Locate and identify every blood parasite.
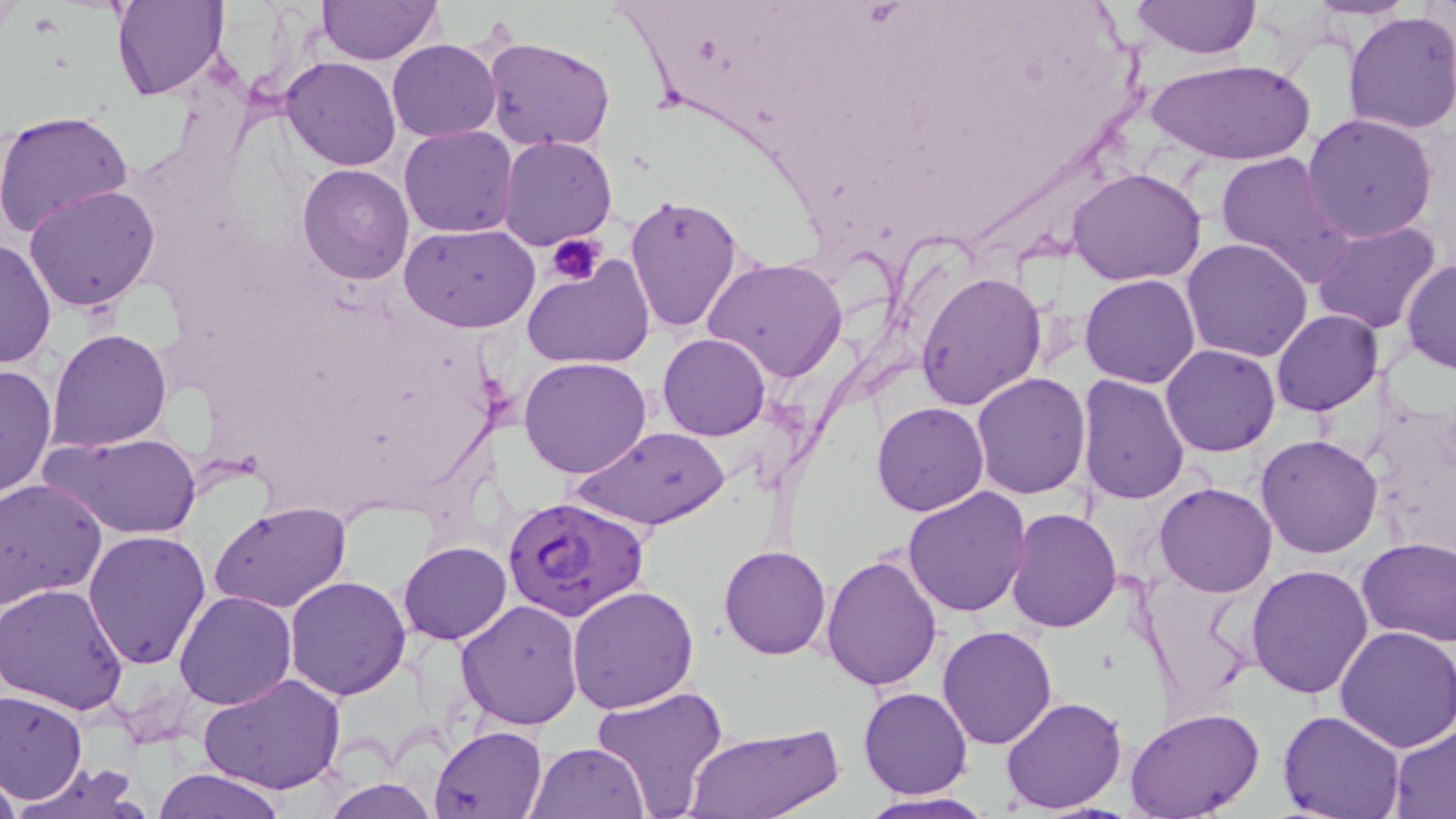

Approximate bounding boxes as named x1/y1/x2/y2 corners in pixels.
Plasmodium falciparum-infected red blood cells: (x1=502, y1=493, x2=651, y2=624).
No Plasmodium ovale, Plasmodium malariae, Plasmodium vivax, Babesia divergens, or Trypanosoma brucei observed.

Uninfected red blood cell locations: (x1=111, y1=1, x2=227, y2=101), (x1=315, y1=1, x2=443, y2=65), (x1=1128, y1=2, x2=1261, y2=59), (x1=1341, y1=10, x2=1456, y2=135), (x1=484, y1=36, x2=617, y2=153), (x1=387, y1=37, x2=501, y2=142), (x1=281, y1=57, x2=401, y2=171), (x1=1145, y1=57, x2=1314, y2=167), (x1=0, y1=108, x2=134, y2=238), (x1=1301, y1=113, x2=1439, y2=243), (x1=399, y1=124, x2=520, y2=237), (x1=498, y1=135, x2=617, y2=250), (x1=1213, y1=151, x2=1356, y2=290), (x1=298, y1=163, x2=414, y2=284), (x1=1067, y1=166, x2=1209, y2=286), (x1=24, y1=185, x2=160, y2=311), (x1=625, y1=193, x2=747, y2=333), (x1=1311, y1=221, x2=1442, y2=335), (x1=400, y1=222, x2=540, y2=333), (x1=0, y1=236, x2=56, y2=371), (x1=1181, y1=237, x2=1314, y2=362), (x1=522, y1=254, x2=656, y2=371), (x1=703, y1=257, x2=848, y2=384), (x1=1401, y1=257, x2=1455, y2=374), (x1=915, y1=270, x2=1048, y2=413), (x1=1079, y1=273, x2=1200, y2=389), (x1=1270, y1=309, x2=1384, y2=415), (x1=49, y1=328, x2=172, y2=451), (x1=658, y1=333, x2=771, y2=441), (x1=1161, y1=344, x2=1282, y2=457), (x1=1096, y1=351, x2=1232, y2=480), (x1=520, y1=357, x2=654, y2=478), (x1=0, y1=362, x2=57, y2=500), (x1=970, y1=372, x2=1091, y2=499), (x1=1077, y1=373, x2=1190, y2=504), (x1=871, y1=401, x2=990, y2=517), (x1=573, y1=425, x2=727, y2=531), (x1=42, y1=431, x2=202, y2=540), (x1=1256, y1=434, x2=1383, y2=557), (x1=0, y1=478, x2=109, y2=610), (x1=1154, y1=482, x2=1278, y2=598), (x1=901, y1=485, x2=1032, y2=616), (x1=210, y1=502, x2=352, y2=614), (x1=1006, y1=508, x2=1122, y2=631), (x1=82, y1=528, x2=214, y2=669), (x1=1357, y1=538, x2=1456, y2=646), (x1=399, y1=541, x2=511, y2=644), (x1=719, y1=543, x2=832, y2=659), (x1=822, y1=550, x2=944, y2=692), (x1=1245, y1=564, x2=1374, y2=700), (x1=285, y1=574, x2=413, y2=700), (x1=0, y1=584, x2=130, y2=714), (x1=568, y1=587, x2=699, y2=714), (x1=174, y1=590, x2=297, y2=710), (x1=454, y1=600, x2=584, y2=731), (x1=937, y1=626, x2=1060, y2=749), (x1=1334, y1=626, x2=1456, y2=751), (x1=197, y1=672, x2=347, y2=795), (x1=592, y1=686, x2=730, y2=816), (x1=858, y1=686, x2=974, y2=800), (x1=1, y1=693, x2=86, y2=802), (x1=999, y1=696, x2=1128, y2=813), (x1=1125, y1=709, x2=1265, y2=819), (x1=1276, y1=710, x2=1405, y2=819), (x1=1389, y1=723, x2=1456, y2=816), (x1=431, y1=726, x2=549, y2=818), (x1=687, y1=727, x2=840, y2=819), (x1=525, y1=741, x2=650, y2=818), (x1=12, y1=764, x2=149, y2=819), (x1=154, y1=767, x2=288, y2=819), (x1=0, y1=771, x2=23, y2=818), (x1=320, y1=777, x2=440, y2=818), (x1=857, y1=792, x2=996, y2=819). Platelet locations: (x1=546, y1=233, x2=605, y2=282). Slide-level diagnosis: Plasmodium falciparum. Image is 1456×819 pixels. Thin blood film. May-Grünwald-Giemsa-stained preparation. Light microscopy. Single field of view. 1000x magnification.